Report the malaria status of this cell.
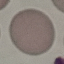
Uninfected.

Thin blood smear. Automatically extracted cell patch, resized to 64 × 64 pixels. Acquired by smartphone through the microscope eyepiece. Giemsa-stained preparation.